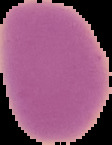 Cell region segmented out of the field of view; the surrounding area is masked to black. Image is 112×145 pixels. From a thin blood film. Malaria status: uninfected.